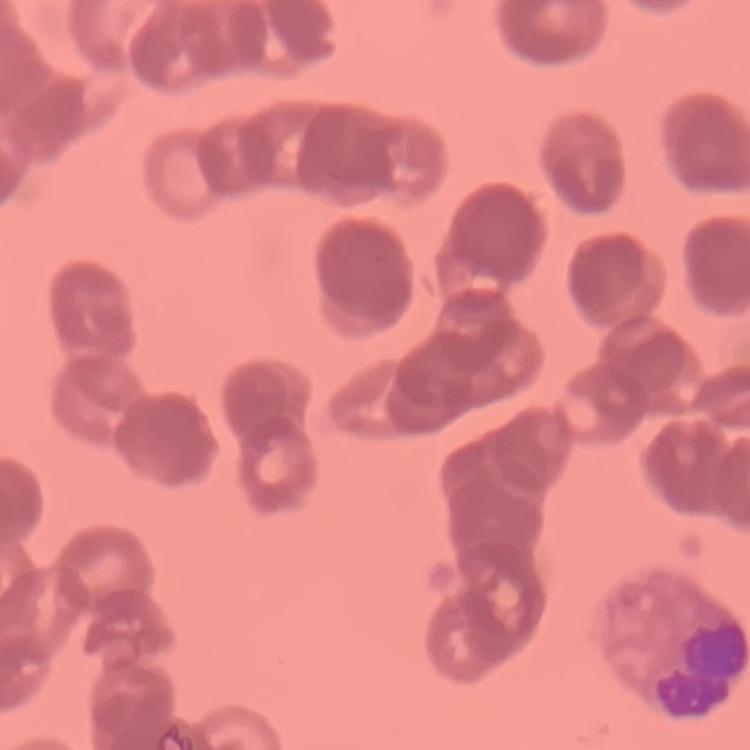

Summary:
  - Red blood cell morphology: rouleaux formation
  - Image type: square crop of a larger photomicrograph
  - Stain: Field's or Giemsa
  - Preparation: thin blood smear